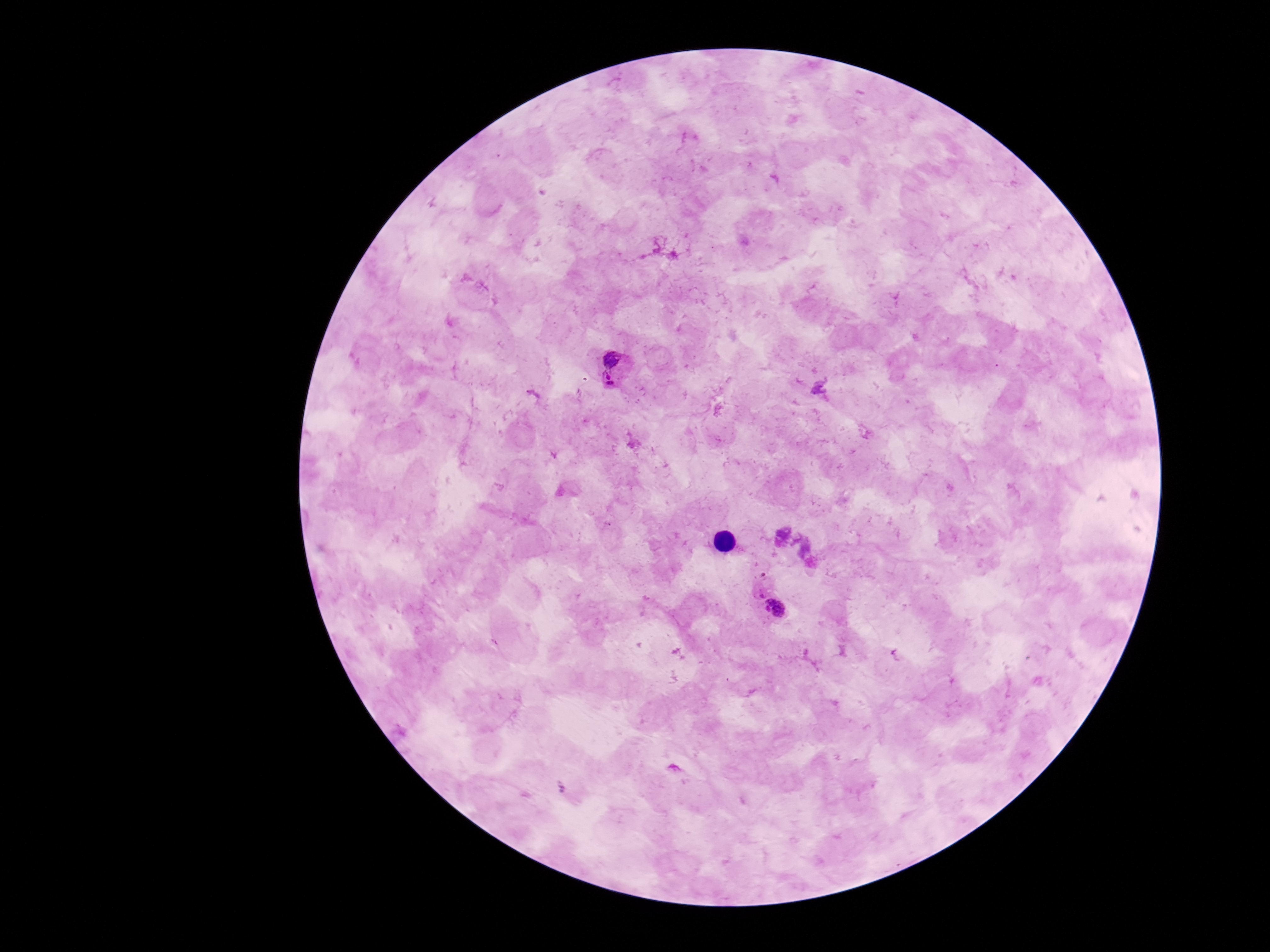

preparation = thick blood smear
Plasmodium parasite locations = approximate object centers, in pixels from the top-left corner: (x=616, y=368), (x=758, y=593), (x=777, y=609)
stain = Giemsa
image size = 1270×952 pixels
capture = smartphone camera through the microscope eyepiece
patient malaria status = infected
magnification = 100x
field of view = single